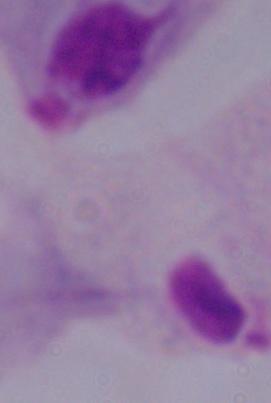
Summary:
  - Modality: photomicrograph
  - Magnification: 1000x
  - Identification: trichomonad